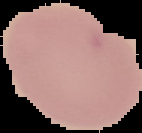
image_type: segmented cell region with the area outside set to black
result: no malaria parasites seen
image_size: 142×133 pixels
preparation: thin blood smear